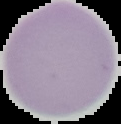

image size = 121×124 pixels
preparation = thin blood smear
image type = segmented cell region on a black background
result = negative for Plasmodium parasites